Report the malaria status of this cell.
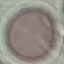
It is uninfected.

Summary:
  - Image type: automatically extracted cell patch, resized to 64 × 64 pixels
  - Capture: smartphone camera at the microscope eyepiece
  - Stain: Giemsa
  - Preparation: thin blood film